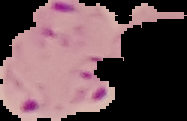 Result: Plasmodium parasites detected. From a thin blood smear. Image is 187×121 pixels. The area outside the segmented cell region is set to black.